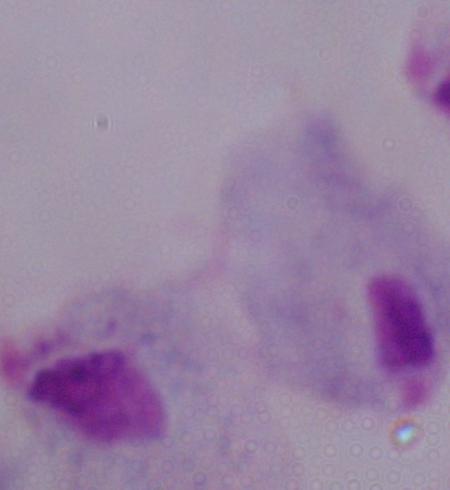
magnification = 1000x
identification = trichomonad
modality = photomicrograph